Name the parasite shown.
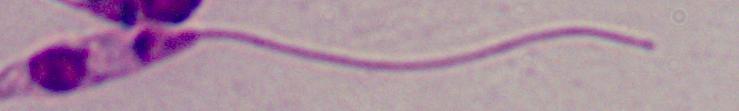

Leishmania.

Summary:
  - Magnification: 1000x
  - Modality: micrograph